Classify this cell by malaria status.
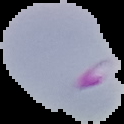
Parasitized.

Summary:
  - Image size: 124×124 pixels
  - Preparation: thin blood film
  - Image type: cell region segmented out of the field of view; surrounding area masked to black